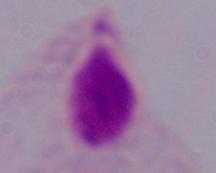

Summary:
  - Magnification: 1000x
  - Modality: photomicrograph
  - Identification: trichomonad